Name the blood parasite species.
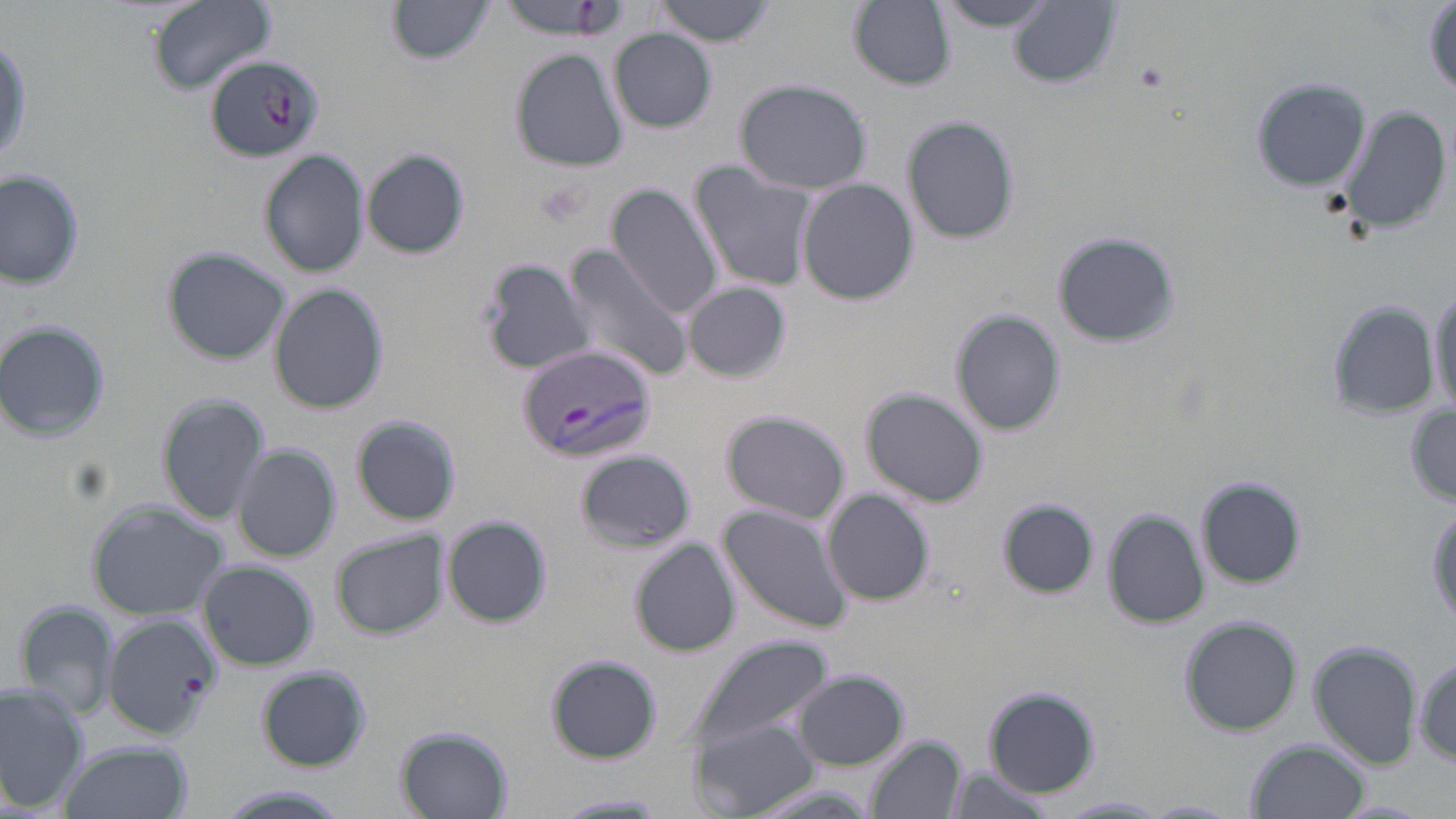
Plasmodium vivax.

Summary:
  - Coordinate format: approximate bounding boxes as (x1, y1, x2, y2) in pixels
  - Plasmodium vivax-infected red blood cell locations: (204, 54, 323, 160), (517, 342, 656, 464)
  - Platelet locations: (1136, 63, 1168, 92)
  - Uninfected red blood cell locations: (147, 0, 278, 93), (497, 0, 616, 36), (655, 0, 776, 45), (935, 0, 1065, 31), (1007, 0, 1120, 88), (849, 1, 958, 90), (389, 2, 501, 65), (1425, 5, 1456, 98), (609, 30, 717, 133), (510, 49, 628, 172), (1252, 76, 1370, 193), (734, 78, 874, 195), (1338, 105, 1450, 233), (901, 114, 1021, 246), (259, 148, 369, 279), (361, 148, 469, 259), (692, 163, 815, 291), (0, 172, 84, 290), (798, 178, 918, 306), (607, 183, 724, 320), (1053, 231, 1178, 347), (561, 244, 696, 383), (162, 246, 290, 364), (479, 255, 593, 378), (1428, 280, 1455, 418), (269, 281, 389, 414), (682, 281, 791, 383), (1325, 304, 1440, 417), (953, 310, 1064, 436), (0, 320, 111, 443), (862, 387, 988, 506), (157, 394, 271, 523), (1407, 405, 1456, 504), (722, 410, 850, 523), (349, 415, 461, 525), (230, 443, 340, 563), (576, 450, 695, 551), (1197, 476, 1308, 589), (821, 488, 935, 606), (1000, 499, 1097, 595), (85, 500, 229, 619), (1427, 500, 1456, 631), (719, 504, 851, 634), (1103, 510, 1207, 629), (442, 517, 550, 628), (330, 530, 448, 639), (630, 540, 740, 657), (200, 561, 318, 671), (15, 599, 122, 722), (101, 614, 220, 739), (1181, 615, 1302, 735), (688, 632, 834, 757), (1310, 641, 1420, 768), (546, 655, 660, 764), (1413, 656, 1455, 764), (258, 667, 370, 772), (794, 670, 910, 770), (0, 683, 87, 815), (984, 684, 1099, 798), (691, 718, 816, 815), (397, 728, 515, 817), (866, 736, 964, 819), (1247, 739, 1370, 819), (59, 740, 191, 819), (551, 794, 671, 817), (1051, 796, 1171, 818)
  - Magnification: 1000x
  - Field of view: one of a larger specimen
  - Stain: May-Grünwald-Giemsa
  - Preparation: thin blood smear
  - Modality: optical microscopy
  - Image size: 1456×819 pixels